State which cell type is depicted.
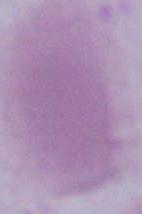

An erythrocyte.

Summary:
  - Modality: photomicrograph
  - Magnification: 1000x